Assess this cell for malaria.
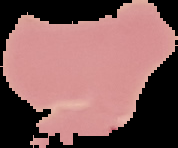

Uninfected.

preparation = thin blood smear
image type = segmented cell region on a black background
image size = 178×148 pixels